State which parasite is depicted.
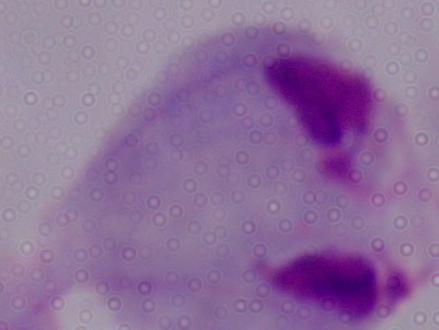
This is a trichomonad.

Summary:
  - Magnification: 1000x
  - Modality: micrograph